Point out each malaria parasite.
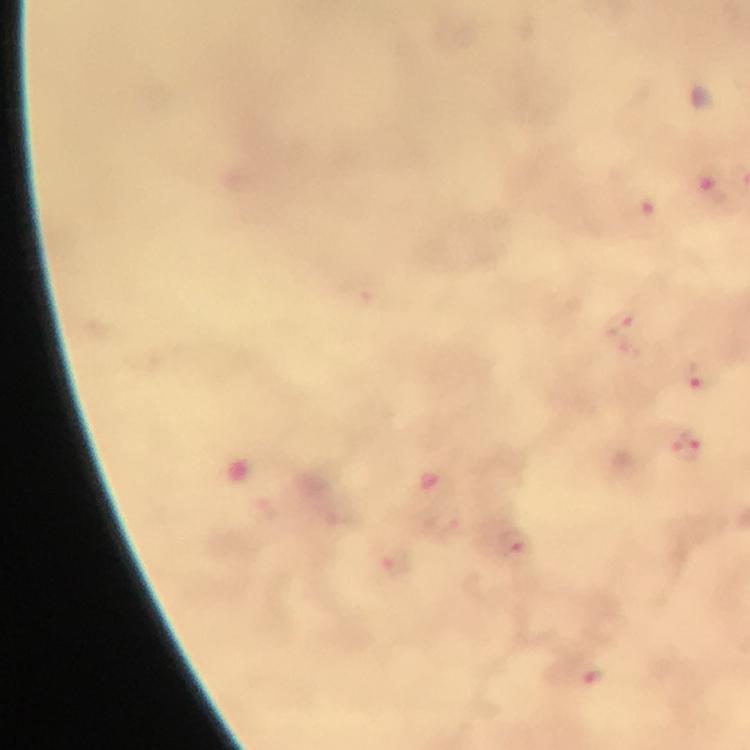

Approximate centers as {x, y} in pixels.
Malaria parasites: {712, 194}, {642, 212}, {624, 326}, {699, 377}, {687, 449}, {513, 540}, {395, 562}, {594, 677}.

Summary:
  - Stain: Giemsa
  - Magnification: 100x
  - Capture: smartphone camera through the microscope
  - Preparation: thick blood smear
  - Cropped from: a single field of view
  - Image size: 750×750 pixels
  - Immersion oil: used
  - Context: from a malaria diagnostic workup